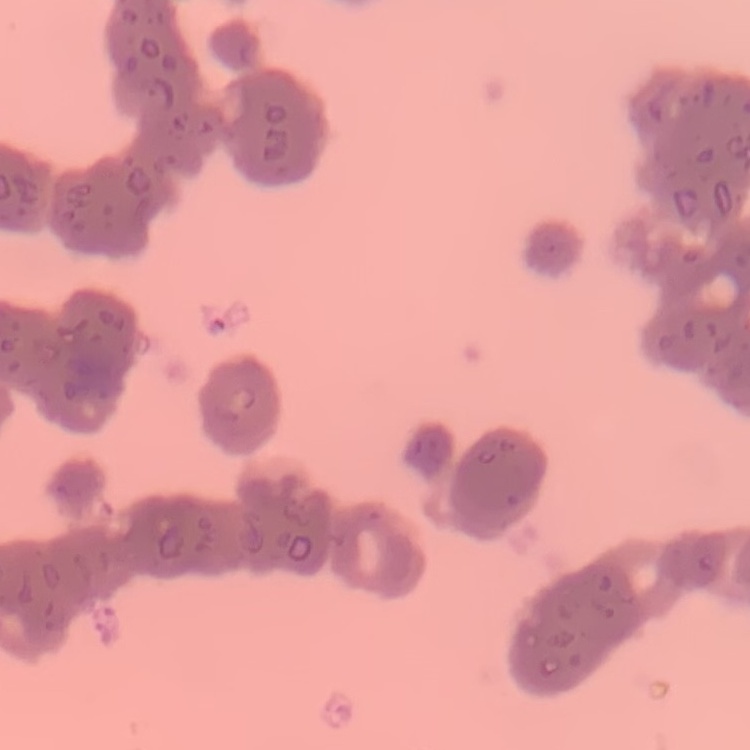
erythrocyte morphology = rouleaux formation
image type = one tile cut from a larger photomicrograph
preparation = thin blood smear
stain = Field's or Giemsa